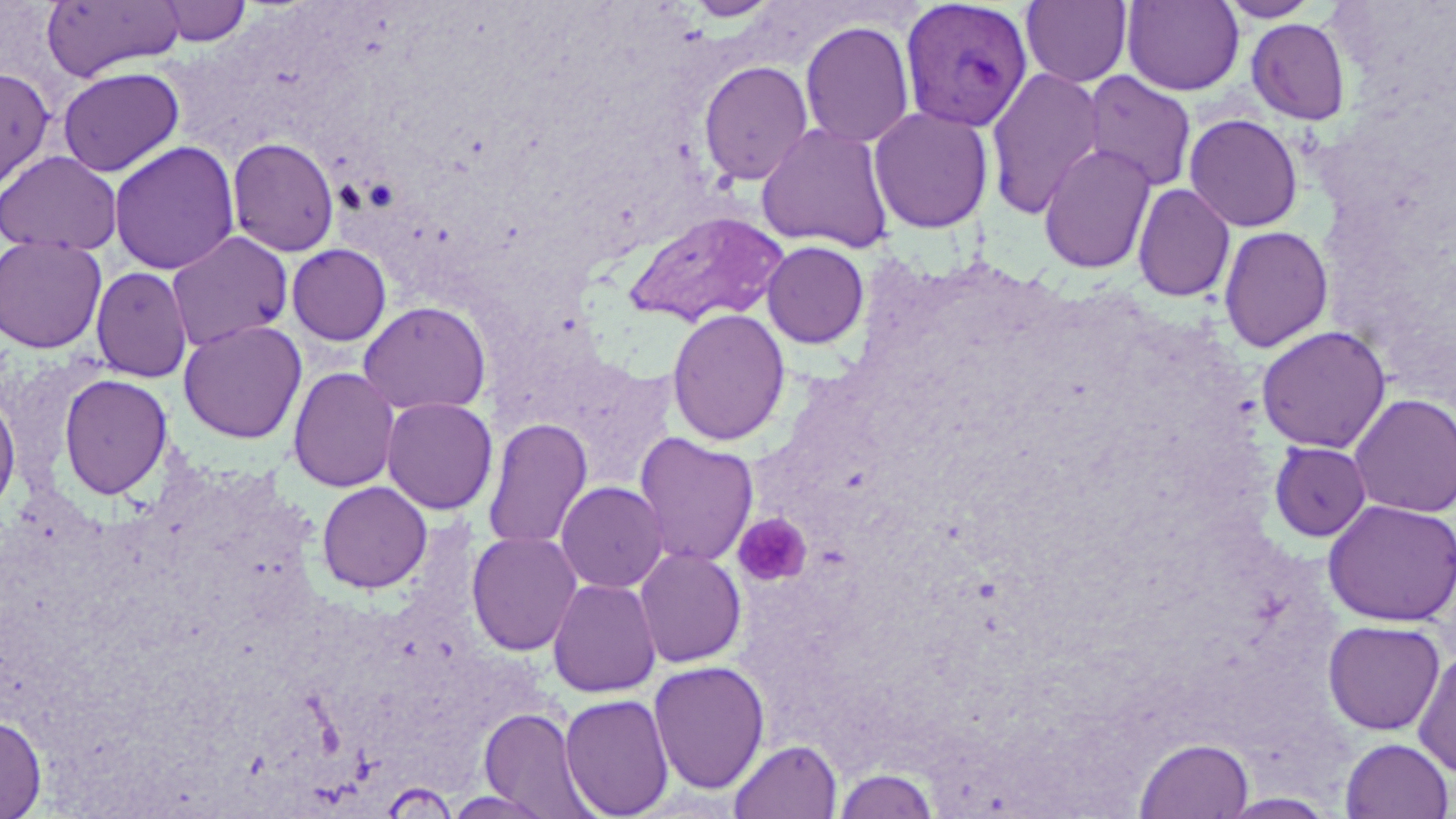
Summary:
  - Coordinate format: approximate bounding boxes as named x1/y1/x2/y2 corners in pixels
  - Plasmodium vivax-infected red blood cell locations: (x1=899, y1=0, x2=1033, y2=133)
  - Platelet locations: (x1=733, y1=512, x2=812, y2=587)
  - Uninfected red blood cell locations: (x1=154, y1=0, x2=252, y2=47), (x1=1020, y1=0, x2=1132, y2=87), (x1=1216, y1=0, x2=1322, y2=23), (x1=40, y1=1, x2=186, y2=82), (x1=685, y1=1, x2=781, y2=22), (x1=1122, y1=1, x2=1245, y2=96), (x1=1246, y1=18, x2=1351, y2=125), (x1=799, y1=20, x2=915, y2=149), (x1=698, y1=60, x2=814, y2=185), (x1=0, y1=66, x2=56, y2=194), (x1=57, y1=66, x2=185, y2=177), (x1=985, y1=66, x2=1106, y2=219), (x1=1081, y1=70, x2=1197, y2=193), (x1=868, y1=106, x2=993, y2=233), (x1=1184, y1=114, x2=1304, y2=232), (x1=756, y1=122, x2=894, y2=253), (x1=227, y1=137, x2=340, y2=256), (x1=108, y1=141, x2=240, y2=275), (x1=1038, y1=143, x2=1157, y2=275), (x1=0, y1=150, x2=123, y2=255), (x1=1132, y1=183, x2=1235, y2=302), (x1=622, y1=210, x2=788, y2=328), (x1=1218, y1=225, x2=1333, y2=353), (x1=166, y1=231, x2=294, y2=352), (x1=0, y1=235, x2=107, y2=353), (x1=762, y1=241, x2=869, y2=349), (x1=286, y1=243, x2=392, y2=346), (x1=90, y1=267, x2=193, y2=382), (x1=358, y1=301, x2=491, y2=416), (x1=666, y1=308, x2=790, y2=446), (x1=178, y1=319, x2=307, y2=444), (x1=1256, y1=325, x2=1391, y2=453), (x1=287, y1=366, x2=400, y2=492), (x1=58, y1=373, x2=173, y2=500), (x1=0, y1=391, x2=21, y2=518), (x1=1349, y1=394, x2=1456, y2=517), (x1=381, y1=397, x2=498, y2=515), (x1=482, y1=418, x2=593, y2=551), (x1=633, y1=432, x2=759, y2=568), (x1=1269, y1=441, x2=1372, y2=541), (x1=316, y1=480, x2=432, y2=594), (x1=555, y1=481, x2=668, y2=594), (x1=1323, y1=499, x2=1456, y2=626), (x1=465, y1=531, x2=583, y2=656), (x1=634, y1=547, x2=747, y2=668), (x1=547, y1=577, x2=661, y2=698), (x1=1323, y1=619, x2=1445, y2=735), (x1=1413, y1=648, x2=1456, y2=778), (x1=648, y1=660, x2=770, y2=795), (x1=559, y1=693, x2=675, y2=818), (x1=479, y1=707, x2=601, y2=819), (x1=0, y1=713, x2=47, y2=819), (x1=1134, y1=736, x2=1255, y2=818), (x1=1340, y1=737, x2=1453, y2=819), (x1=729, y1=739, x2=843, y2=819), (x1=832, y1=765, x2=939, y2=819), (x1=443, y1=790, x2=559, y2=818), (x1=1217, y1=793, x2=1339, y2=818)
  - Slide-level diagnosis: Plasmodium vivax
  - Field of view: one of a larger specimen
  - Stain: May-Grünwald-Giemsa
  - Modality: light microscopy
  - Magnification: 1000x
  - Image size: 1456×819 pixels
  - Preparation: thin blood smear